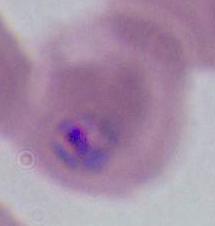
Summary:
  - Identification: Plasmodium
  - Magnification: 400x or 1000x
  - Modality: photomicrograph